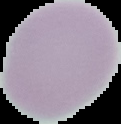
Summary:
  - Result: no Plasmodium parasites seen
  - Image type: cell region segmented out of the field of view; surrounding area masked to black
  - Preparation: thin blood smear
  - Image size: 121×124 pixels